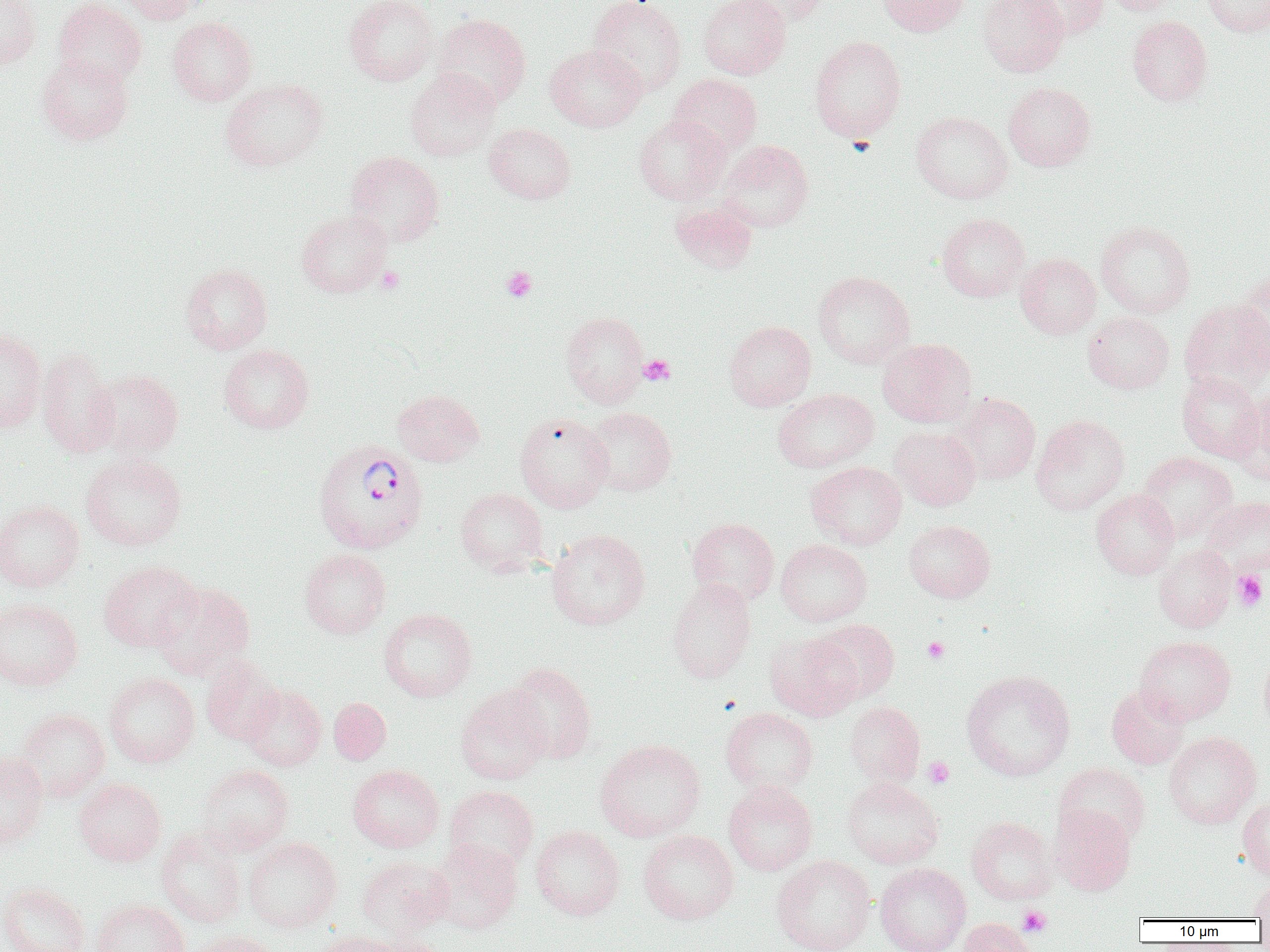
Plasmodium vivax-infected red blood cell locations = approximate bounding boxes as (x1,y1)-(x2,y2) corner pairs in pixels: (312,438)-(427,554)
slide-level diagnosis = Plasmodium vivax
preparation = thin blood smear
field of view = one of a larger specimen
image size = 1270×952 pixels
magnification = 1000x
platelet locations = approximate bounding boxes as (x1,y1)-(x2,y2) corner pairs in pixels: (376,266)-(404,294), (501,266)-(537,302), (639,354)-(675,385), (1231,570)-(1267,611), (923,637)-(949,663), (923,757)-(955,789), (1017,906)-(1052,937)
uninfected red blood cell locations = approximate bounding boxes as (x1,y1)-(x2,y2) corner pairs in pixels: (0,0)-(40,70), (53,0)-(146,87), (115,0)-(205,24), (343,0)-(439,86), (588,0)-(686,96), (698,0)-(791,79), (733,0)-(829,26), (877,0)-(971,36), (978,0)-(1069,77), (1020,0)-(1108,40), (1104,0)-(1186,15), (1201,0)-(1270,37), (432,13)-(531,108), (168,16)-(257,105), (1128,16)-(1213,105), (809,35)-(906,142), (545,44)-(646,132), (37,54)-(133,145), (405,69)-(501,161), (669,73)-(762,157), (220,78)-(328,172), (1003,82)-(1096,172), (911,110)-(1013,203), (634,114)-(730,204), (484,122)-(576,204), (716,140)-(814,232), (344,151)-(444,247), (670,202)-(759,274), (296,209)-(392,298), (936,213)-(1030,302), (1095,220)-(1196,318), (1015,253)-(1101,339), (180,263)-(272,354), (813,270)-(915,368), (1234,272)-(1270,372), (1179,298)-(1270,394), (560,311)-(649,407), (1083,311)-(1174,394), (724,320)-(816,411), (0,327)-(47,432), (877,338)-(977,427), (219,344)-(314,433), (37,347)-(119,458), (87,369)-(184,460), (1177,372)-(1265,462), (772,388)-(879,472), (392,389)-(484,467), (1231,389)-(1270,488), (951,392)-(1040,484), (582,407)-(676,496), (515,413)-(613,512), (1031,413)-(1130,516), (889,425)-(981,510), (1138,451)-(1237,541), (80,453)-(187,551), (806,461)-(907,550), (455,487)-(549,576), (1091,489)-(1180,579), (1201,496)-(1270,574), (0,499)-(85,592), (687,517)-(779,606), (904,520)-(995,602), (546,529)-(650,630), (775,539)-(872,626), (1154,545)-(1235,633), (299,548)-(391,638), (98,561)-(200,652), (666,577)-(756,683), (151,581)-(255,679), (0,597)-(83,692), (378,608)-(477,702), (812,618)-(900,702), (765,632)-(861,722), (1134,636)-(1235,724), (1258,650)-(1270,734), (200,655)-(282,745), (504,662)-(597,764), (961,669)-(1075,781), (104,673)-(199,767), (241,684)-(327,770), (1107,685)-(1190,769), (455,686)-(552,784), (329,698)-(391,765), (844,701)-(925,788), (721,707)-(818,796), (14,708)-(110,802), (1163,731)-(1261,829), (595,738)-(705,842), (0,751)-(49,850), (1054,763)-(1151,848), (196,764)-(294,855), (348,764)-(444,852), (73,777)-(166,867), (842,777)-(944,869), (723,782)-(817,876), (444,785)-(539,874), (1237,798)-(1270,881), (1049,803)-(1135,895), (966,816)-(1059,904), (530,825)-(625,920), (156,828)-(246,927), (638,830)-(738,924), (244,837)-(341,933), (429,838)-(522,934), (772,855)-(876,952), (356,856)-(454,938), (875,863)-(971,952), (1249,881)-(1270,920), (0,882)-(89,952), (93,899)-(188,952), (960,918)-(1037,952), (188,929)-(283,952), (312,930)-(405,952), (371,933)-(451,952)
modality = light microscopy